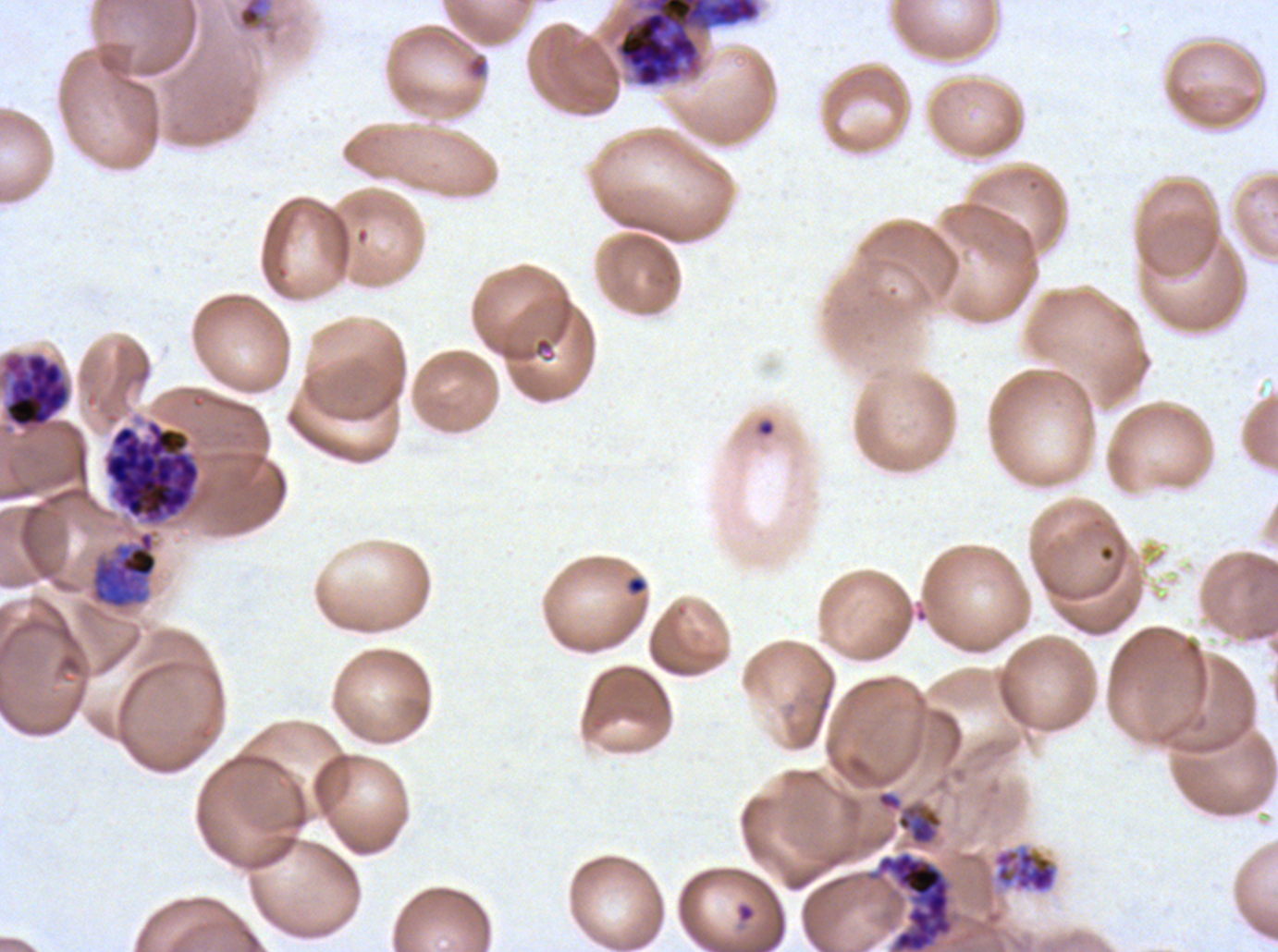 Approximate bounding boxes as {x1, y1, x2, y2} in pixels. Ring locations: {627, 576, 646, 594}, {736, 901, 756, 923}. Late trophozoite locations: {89, 529, 159, 611}. Debris locations: {237, 0, 268, 31}, {465, 52, 489, 80}. Late schizont locations: {4, 353, 69, 428}, {103, 420, 201, 524}. Early schizont locations: {616, 0, 760, 87}. Mid trophozoite locations: {875, 789, 945, 848}, {991, 843, 1059, 895}. Giemsa-stained preparation. Life-cycle stages observed: ring, mid trophozoite, late trophozoite, early schizont, late schizont. Image is 1278×952 pixels. One sub-image of a larger composite. Thin blood smear. Ex-vivo Plasmodium falciparum culture from a patient in The Gambia, grown for 24 to 48 hours.